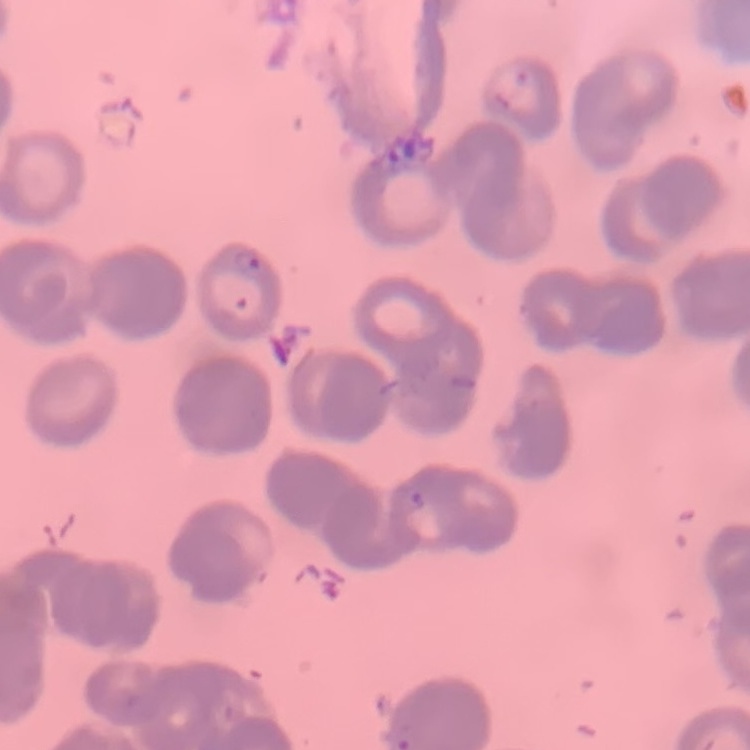
erythrocyte morphology = rouleaux formation
image type = one tile cut from a larger photomicrograph
stain = Field's or Giemsa
preparation = thin blood film